Outline each Plasmodium falciparum-infected red blood cell.
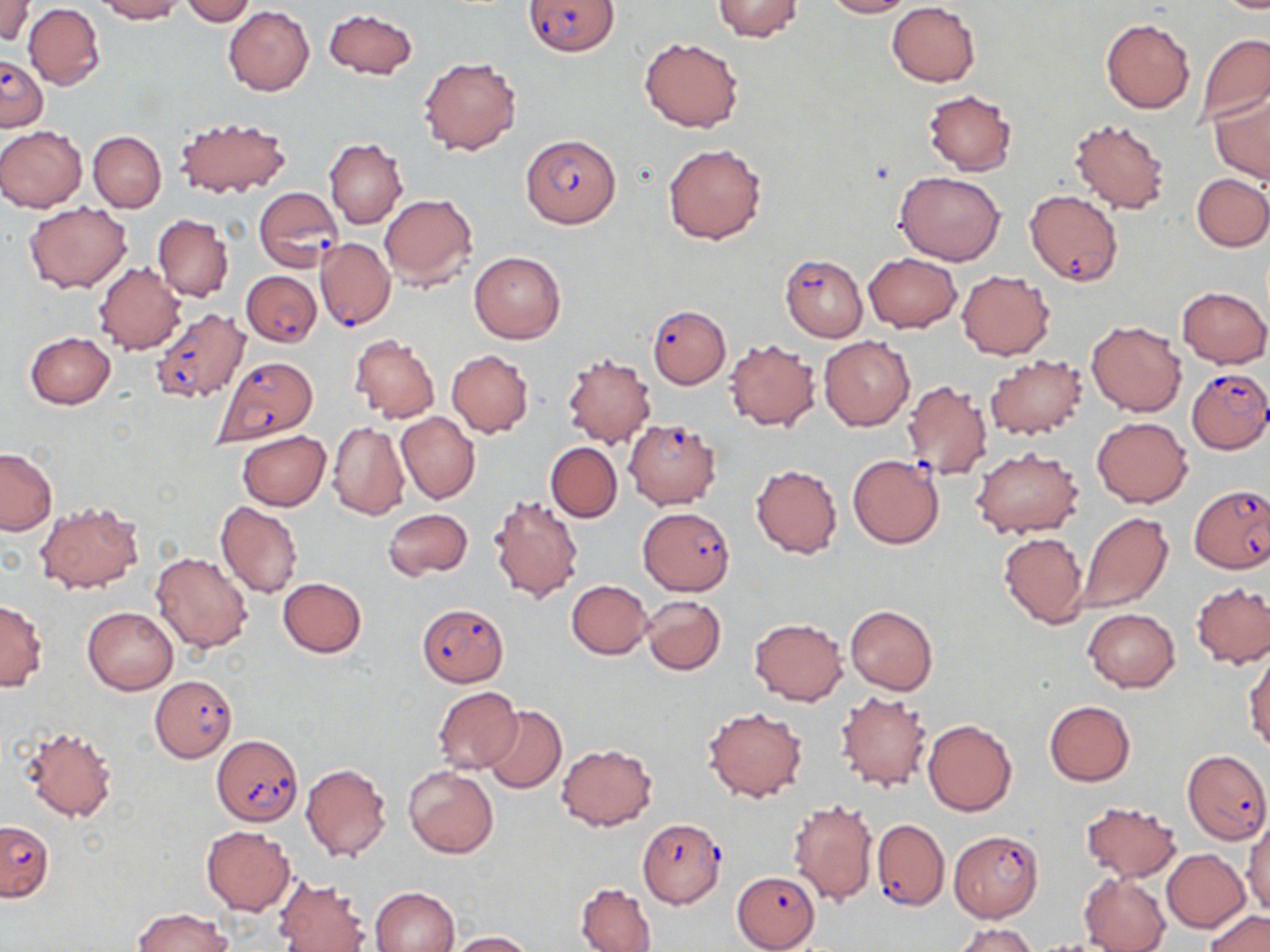

Approximate bounding boxes as named x1/y1/x2/y2 corners in pixels.
Plasmodium falciparum-infected red blood cells: (x1=522, y1=0, x2=618, y2=56), (x1=1, y1=55, x2=48, y2=129), (x1=519, y1=133, x2=622, y2=228), (x1=254, y1=186, x2=342, y2=275), (x1=1024, y1=190, x2=1123, y2=286), (x1=315, y1=237, x2=395, y2=331), (x1=780, y1=255, x2=867, y2=341), (x1=241, y1=271, x2=321, y2=345), (x1=648, y1=306, x2=730, y2=388), (x1=149, y1=307, x2=249, y2=403), (x1=213, y1=356, x2=318, y2=445), (x1=1186, y1=368, x2=1270, y2=453), (x1=624, y1=419, x2=720, y2=509), (x1=847, y1=454, x2=945, y2=548), (x1=1190, y1=485, x2=1268, y2=574), (x1=638, y1=507, x2=734, y2=595), (x1=417, y1=602, x2=510, y2=686), (x1=149, y1=676, x2=237, y2=760), (x1=212, y1=735, x2=303, y2=825), (x1=1183, y1=749, x2=1270, y2=844), (x1=873, y1=817, x2=949, y2=911), (x1=639, y1=818, x2=727, y2=908), (x1=0, y1=821, x2=53, y2=901), (x1=951, y1=830, x2=1043, y2=921), (x1=732, y1=870, x2=821, y2=950).

slide-level diagnosis = Plasmodium falciparum
magnification = 1000x
image size = 1270×952 pixels
field of view = single
stain = May-Grünwald-Giemsa
modality = light microscopy
preparation = thin blood film
uninfected red blood cell locations = approximate bounding boxes as named x1/y1/x2/y2 corners in pixels: (x1=1, y1=0, x2=33, y2=44), (x1=93, y1=0, x2=183, y2=22), (x1=179, y1=0, x2=256, y2=25), (x1=711, y1=0, x2=803, y2=41), (x1=821, y1=0, x2=912, y2=18), (x1=1211, y1=0, x2=1270, y2=12), (x1=886, y1=2, x2=980, y2=86), (x1=24, y1=4, x2=104, y2=89), (x1=223, y1=5, x2=315, y2=96), (x1=324, y1=8, x2=417, y2=79), (x1=1101, y1=18, x2=1194, y2=114), (x1=1196, y1=33, x2=1270, y2=124), (x1=639, y1=37, x2=743, y2=132), (x1=418, y1=56, x2=523, y2=156), (x1=924, y1=89, x2=1017, y2=175), (x1=1210, y1=91, x2=1270, y2=185), (x1=1069, y1=116, x2=1172, y2=215), (x1=175, y1=117, x2=291, y2=198), (x1=0, y1=125, x2=87, y2=212), (x1=88, y1=130, x2=166, y2=213), (x1=325, y1=138, x2=408, y2=229), (x1=664, y1=143, x2=766, y2=244), (x1=894, y1=171, x2=1004, y2=265), (x1=1193, y1=172, x2=1270, y2=251), (x1=380, y1=193, x2=477, y2=289), (x1=25, y1=203, x2=130, y2=294), (x1=153, y1=213, x2=233, y2=302), (x1=469, y1=251, x2=566, y2=343), (x1=863, y1=252, x2=962, y2=332), (x1=93, y1=262, x2=185, y2=354), (x1=957, y1=270, x2=1054, y2=359), (x1=1177, y1=286, x2=1270, y2=368), (x1=1087, y1=320, x2=1187, y2=416), (x1=24, y1=332, x2=115, y2=408), (x1=349, y1=335, x2=441, y2=422), (x1=818, y1=336, x2=915, y2=430), (x1=724, y1=338, x2=820, y2=431), (x1=446, y1=349, x2=534, y2=438), (x1=562, y1=353, x2=655, y2=449), (x1=984, y1=355, x2=1087, y2=439), (x1=901, y1=378, x2=993, y2=481), (x1=395, y1=412, x2=480, y2=505), (x1=1092, y1=417, x2=1191, y2=507), (x1=328, y1=421, x2=410, y2=521), (x1=236, y1=431, x2=331, y2=511), (x1=545, y1=442, x2=622, y2=522), (x1=971, y1=448, x2=1082, y2=538), (x1=0, y1=449, x2=57, y2=535), (x1=751, y1=463, x2=842, y2=558), (x1=488, y1=494, x2=583, y2=602), (x1=35, y1=500, x2=144, y2=593), (x1=215, y1=501, x2=302, y2=599), (x1=383, y1=507, x2=473, y2=580), (x1=1076, y1=512, x2=1172, y2=612), (x1=998, y1=532, x2=1089, y2=627), (x1=150, y1=552, x2=252, y2=654), (x1=277, y1=577, x2=366, y2=658), (x1=566, y1=580, x2=652, y2=659), (x1=1191, y1=582, x2=1270, y2=668), (x1=640, y1=594, x2=727, y2=674), (x1=0, y1=599, x2=47, y2=690), (x1=845, y1=605, x2=937, y2=695), (x1=82, y1=606, x2=178, y2=694), (x1=1083, y1=608, x2=1179, y2=692), (x1=750, y1=618, x2=847, y2=706), (x1=1244, y1=650, x2=1270, y2=753), (x1=432, y1=686, x2=521, y2=774), (x1=834, y1=691, x2=931, y2=791), (x1=1044, y1=701, x2=1135, y2=785), (x1=703, y1=705, x2=807, y2=802), (x1=482, y1=706, x2=566, y2=794), (x1=924, y1=719, x2=1017, y2=816), (x1=20, y1=723, x2=120, y2=822), (x1=555, y1=743, x2=657, y2=831), (x1=300, y1=763, x2=391, y2=861), (x1=402, y1=767, x2=498, y2=858), (x1=788, y1=798, x2=879, y2=906), (x1=1080, y1=800, x2=1182, y2=883), (x1=1243, y1=818, x2=1270, y2=916), (x1=201, y1=825, x2=296, y2=914), (x1=1162, y1=848, x2=1250, y2=933), (x1=1078, y1=873, x2=1171, y2=952), (x1=275, y1=878, x2=370, y2=952), (x1=575, y1=881, x2=656, y2=952), (x1=371, y1=886, x2=458, y2=952), (x1=134, y1=908, x2=232, y2=951), (x1=1204, y1=909, x2=1269, y2=952), (x1=954, y1=922, x2=1038, y2=952), (x1=447, y1=931, x2=533, y2=951)